Outline each Plasmodium falciparum-infected red blood cell.
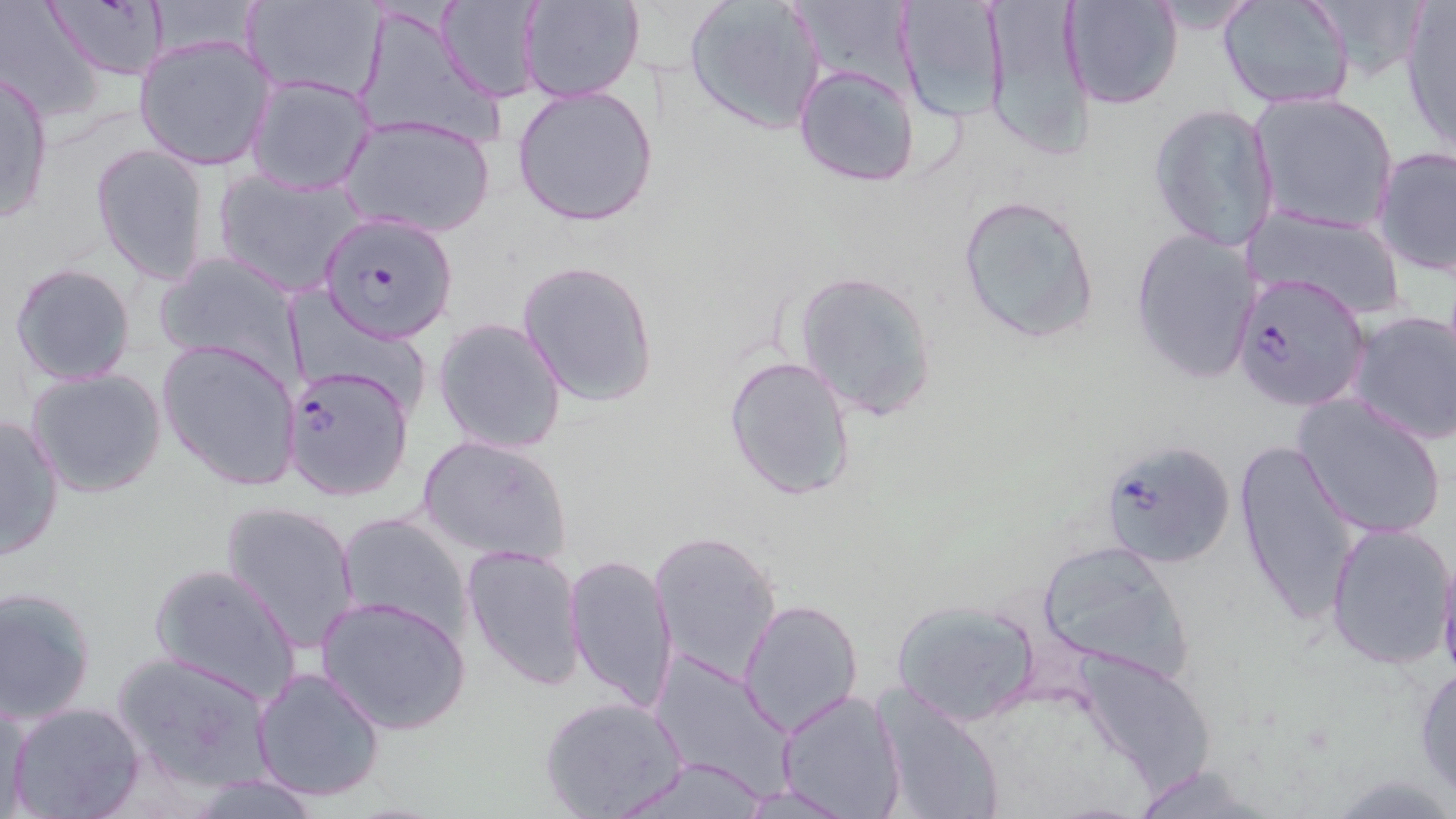

Approximate bounding boxes as (x1, y1, x2, y2) in pixels.
Plasmodium falciparum-infected red blood cells: (318, 212, 459, 344), (1232, 271, 1370, 413), (284, 364, 416, 501).

Uninfected red blood cell locations: (241, 0, 387, 102), (519, 0, 645, 104), (788, 0, 908, 93), (896, 0, 1007, 130), (980, 0, 1095, 162), (1060, 0, 1183, 111), (1299, 0, 1432, 81), (435, 1, 542, 103), (684, 1, 826, 134), (1218, 1, 1355, 111), (42, 2, 173, 81), (1398, 2, 1456, 158), (0, 3, 110, 120), (355, 8, 505, 152), (135, 35, 276, 171), (792, 64, 922, 187), (0, 72, 54, 223), (247, 73, 377, 197), (512, 84, 660, 228), (1248, 91, 1399, 236), (1148, 102, 1280, 251), (340, 114, 497, 238), (90, 143, 213, 285), (1372, 146, 1456, 277), (213, 166, 369, 298), (956, 194, 1099, 345), (1243, 205, 1408, 319), (1130, 227, 1263, 384), (155, 252, 303, 382), (515, 259, 660, 407), (10, 261, 137, 386), (793, 269, 939, 421), (284, 287, 420, 405), (1348, 309, 1456, 446), (433, 317, 567, 455), (157, 338, 302, 491), (723, 353, 859, 500), (26, 367, 169, 499), (1294, 395, 1446, 539), (0, 414, 65, 560), (417, 434, 574, 567), (1098, 439, 1236, 570), (1234, 440, 1358, 626), (219, 498, 362, 653), (336, 511, 473, 644), (1324, 519, 1456, 671), (648, 529, 782, 688), (1034, 538, 1197, 682), (461, 543, 587, 693), (1437, 546, 1456, 690), (564, 552, 678, 719), (149, 561, 304, 707), (1, 587, 100, 724), (314, 595, 471, 737), (738, 598, 865, 734), (890, 598, 1043, 726), (1069, 647, 1215, 794), (111, 650, 276, 791), (647, 651, 794, 791), (1414, 661, 1456, 802), (249, 665, 387, 801), (777, 688, 908, 819), (871, 688, 1005, 819), (540, 696, 687, 818), (0, 698, 33, 818), (7, 700, 145, 819), (613, 753, 771, 819), (1122, 763, 1281, 818). Slide-level diagnosis: Plasmodium falciparum. Thin blood film. May-Grünwald-Giemsa stain. Light microscopy. One field of a larger specimen. Image is 1456×819 pixels. 1000x magnification.